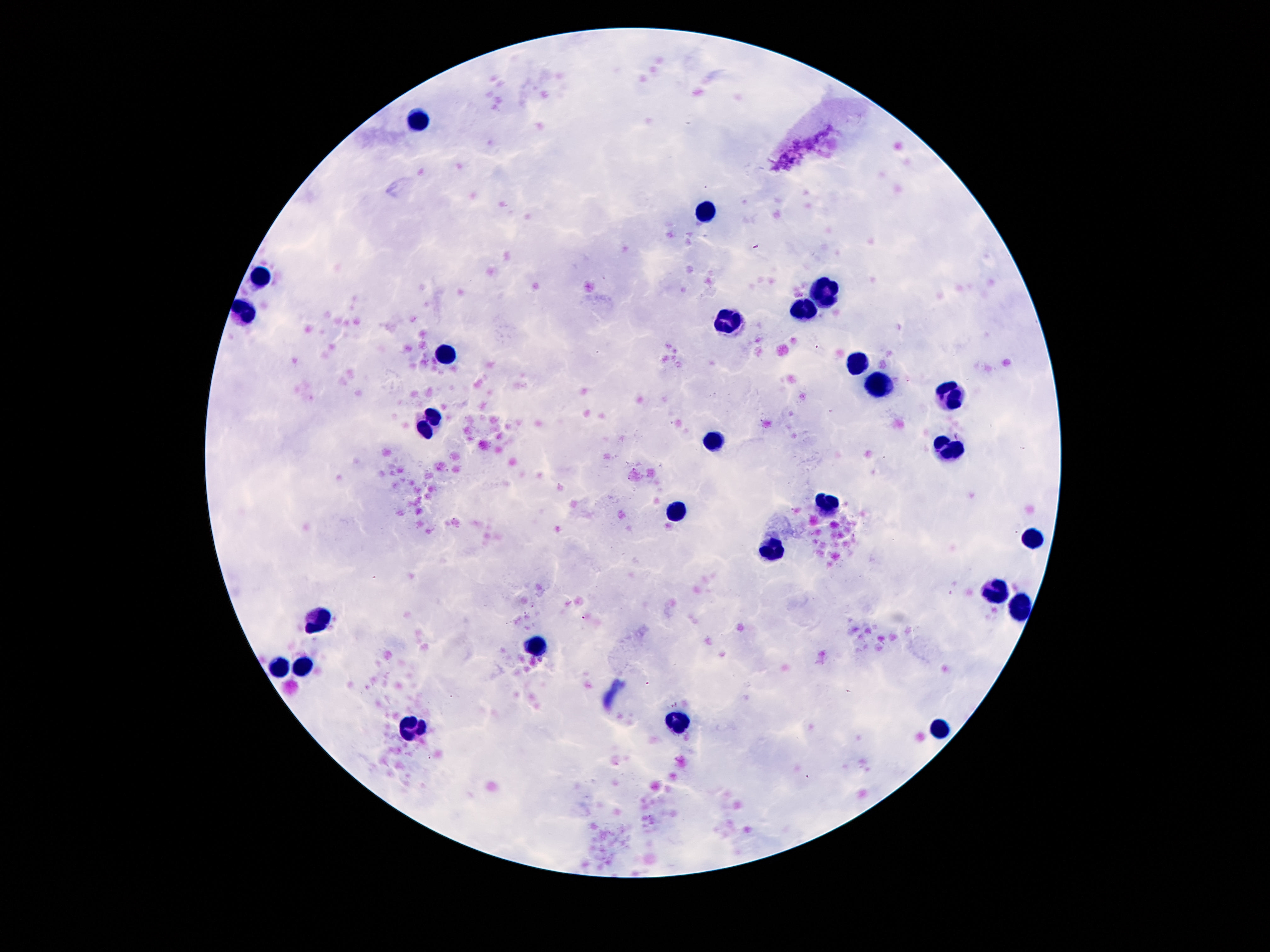 Approximate centers as [x, y] in pixels. Leukocyte locations: [423, 120], [706, 212], [261, 277], [825, 292], [806, 310], [243, 313], [729, 321], [446, 353], [858, 363], [878, 382], [950, 394], [431, 425], [716, 442], [948, 449], [825, 501], [673, 509], [1032, 540], [772, 549], [997, 590], [1021, 604], [319, 620], [538, 644], [282, 665], [303, 665], [679, 723], [413, 728], [940, 731]. Single field of view. 100x magnification. Photographed through the microscope eyepiece with a smartphone camera. Giemsa-stained preparation. Patient malaria status: not infected. Image is 1270×952 pixels. Thick blood film.